Point out each leukocyte.
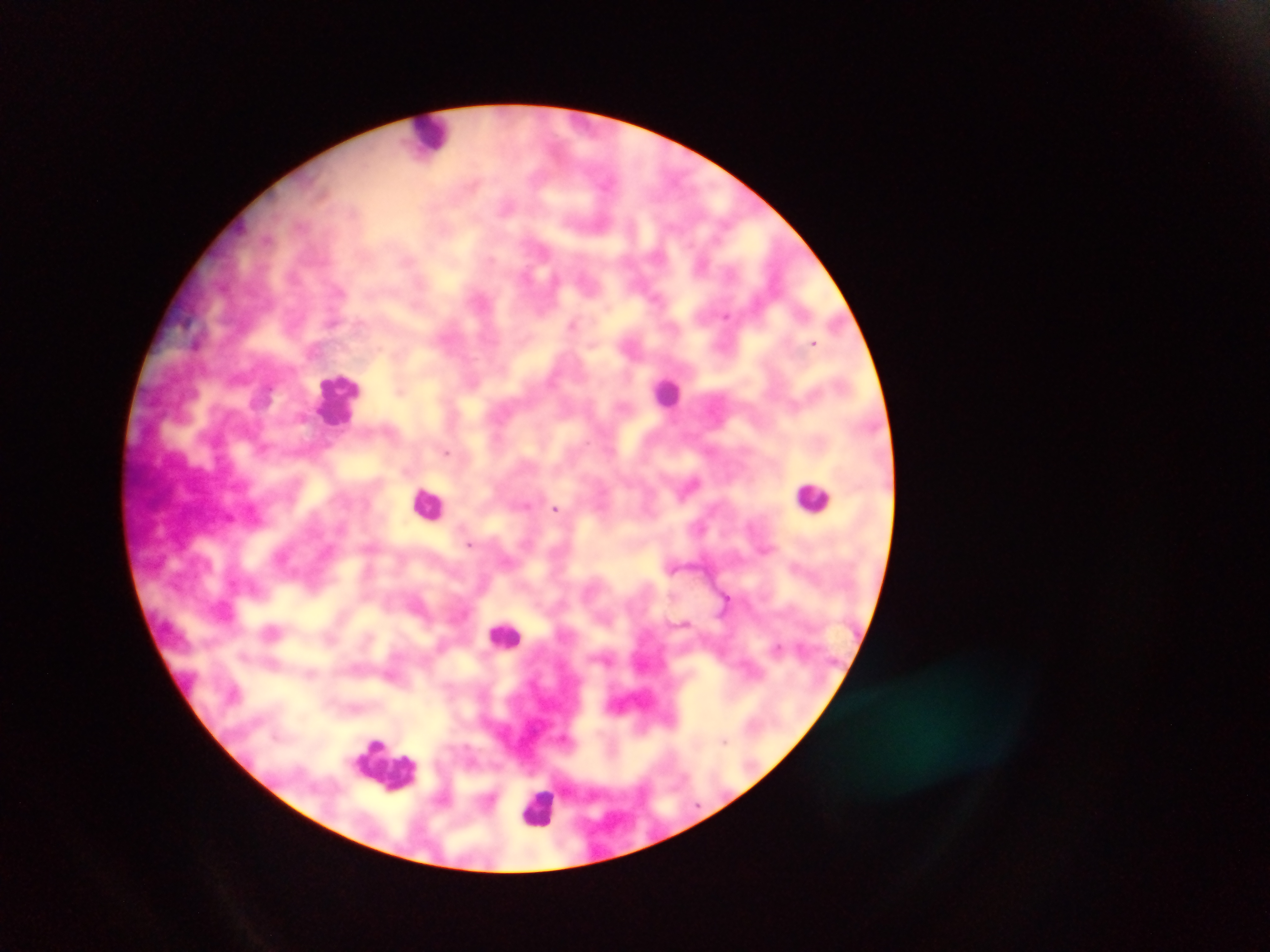
Approximate centers as [x, y] in pixels.
Leukocytes: [430, 136], [668, 392], [340, 400], [813, 497], [428, 503], [504, 633], [183, 680], [385, 763], [537, 808].

Malaria parasite locations: [701, 263], [727, 314], [573, 324], [815, 343], [401, 388], [446, 452], [691, 484], [527, 504], [556, 509], [470, 544], [726, 599], [725, 740]. Mobile-phone photograph taken through the microscope. Thick blood smear. Image is 1270×952 pixels. Sample from Ghana. One field of view.